Outline every leukocyte.
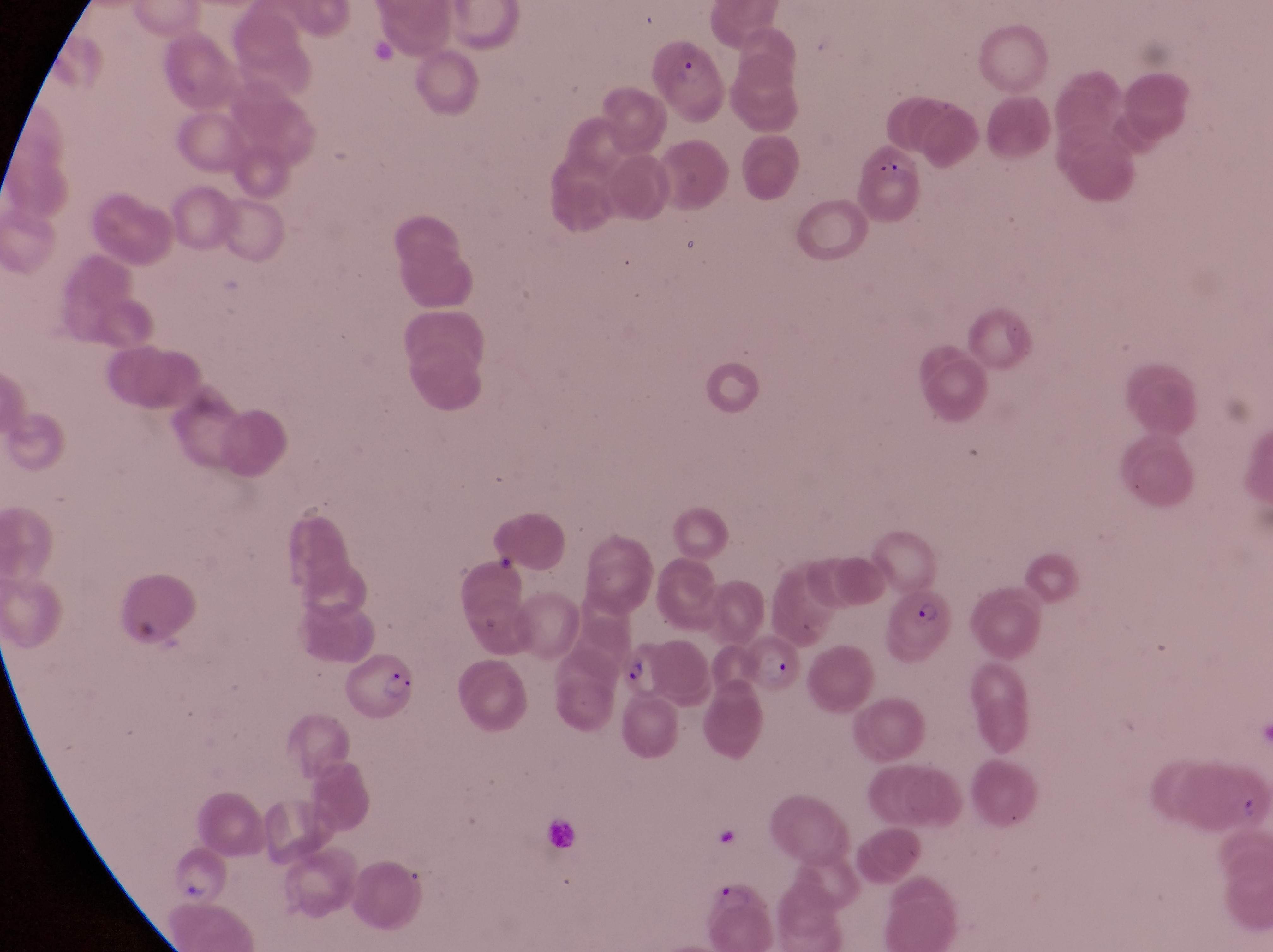
No leukocytes observed.

Approximate bounding boxes as (left, top, right, bottom) in pixels. Parasitised red blood cell locations: (645, 42, 726, 125), (893, 587, 967, 659), (747, 632, 805, 689), (626, 642, 674, 699), (340, 652, 415, 719), (704, 881, 781, 944). One field of view. Sample from Uganda. Thin blood smear. At a magnification of 1000x. Image is 1273×952 pixels. Photographed through the eyepiece of an Olympus CX-23 microscope with a smartphone camera.